State which parasite is depicted.
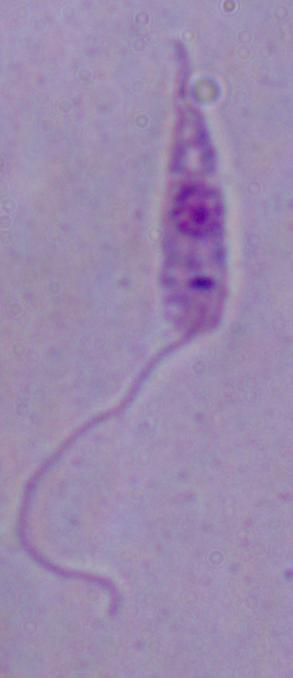

Leishmania.

Photomicrograph. Captured at 1000x magnification.